State which parasite is depicted.
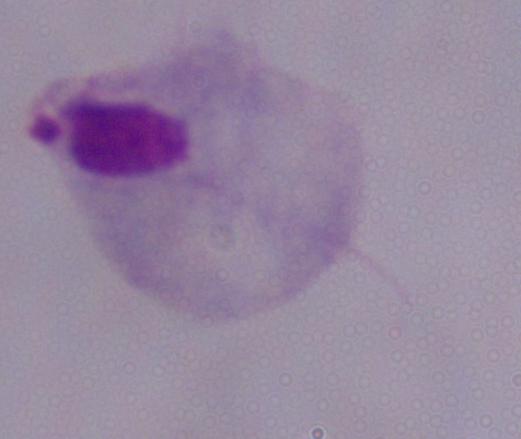
A trichomonad.

Summary:
  - Magnification: 1000x
  - Modality: photomicrograph